Assess this cell for malaria.
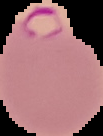

Parasitized.

Summary:
  - Image size: 103×136 pixels
  - Image type: segmented cell region on a black background
  - Preparation: thin blood smear